Locate every blood parasite and identify its species.
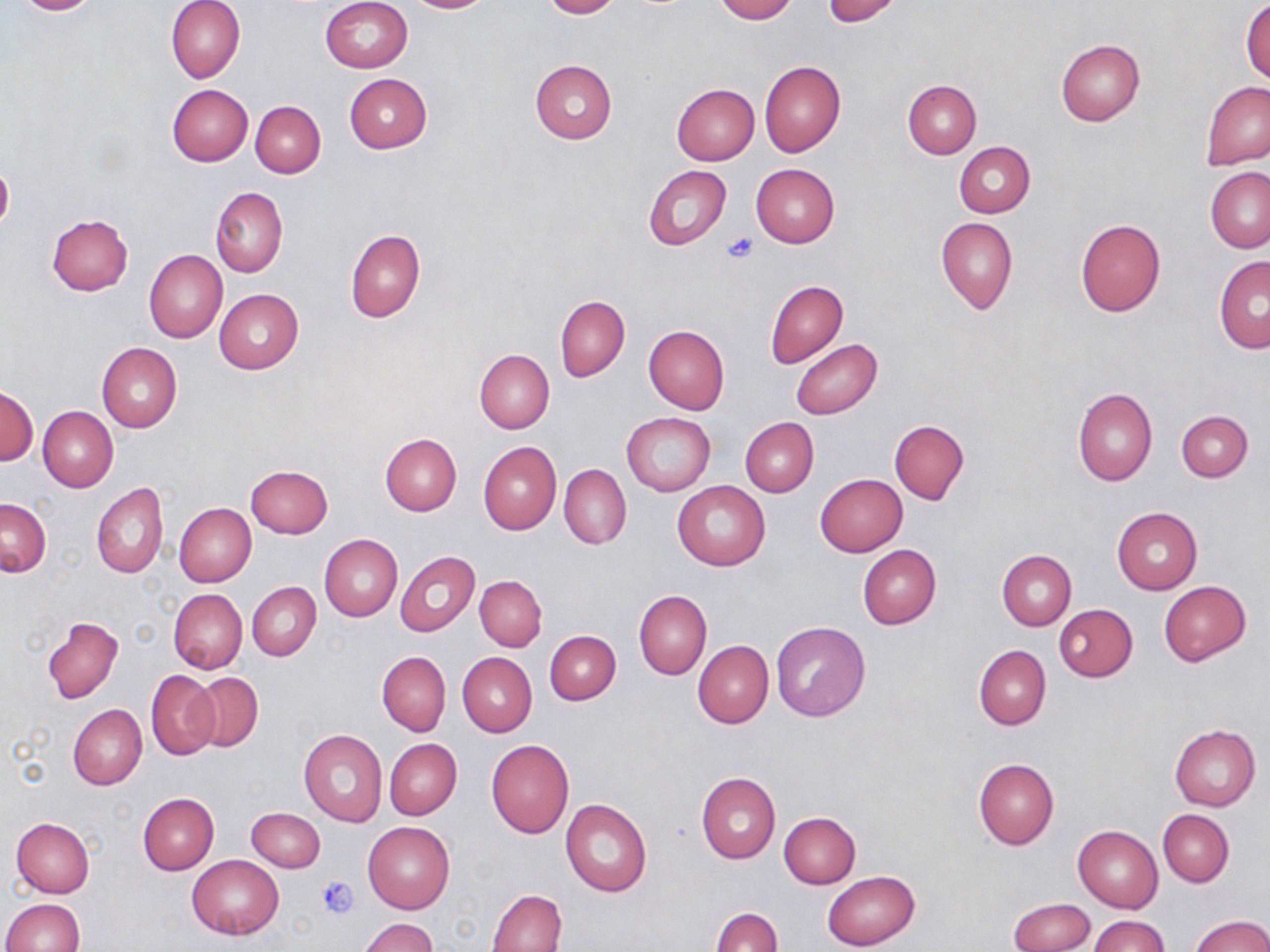
No blood parasites seen.

Approximate bounding boxes as (x1, y1, x2, y2) in pixels. Platelet locations: (722, 232, 759, 264), (317, 874, 359, 917). Uninfected red blood cell locations: (11, 0, 103, 15), (166, 0, 245, 83), (320, 0, 413, 73), (404, 0, 494, 14), (540, 0, 621, 19), (713, 0, 797, 22), (823, 0, 902, 25), (1241, 2, 1270, 83), (1054, 39, 1143, 126), (530, 60, 617, 144), (759, 61, 845, 157), (343, 74, 431, 154), (902, 80, 981, 159), (1201, 82, 1270, 170), (167, 84, 253, 166), (672, 84, 760, 165), (250, 100, 325, 178), (955, 142, 1035, 218), (0, 162, 14, 231), (750, 163, 839, 247), (644, 165, 731, 250), (1206, 168, 1270, 253), (210, 186, 288, 277), (47, 215, 133, 295), (936, 217, 1018, 313), (1075, 219, 1165, 317), (345, 229, 425, 323), (144, 249, 227, 343), (1213, 257, 1270, 354), (765, 280, 847, 368), (214, 289, 303, 374), (555, 295, 630, 381), (643, 325, 729, 415), (790, 339, 883, 418), (97, 343, 181, 433), (474, 348, 555, 433), (0, 386, 38, 465), (1072, 388, 1157, 486), (37, 406, 117, 492), (1177, 410, 1252, 482), (623, 412, 714, 497), (741, 417, 819, 497), (890, 419, 969, 506), (380, 434, 461, 515), (478, 441, 561, 535), (560, 464, 631, 550), (245, 465, 333, 538), (815, 473, 907, 557), (673, 480, 770, 571), (91, 483, 168, 578), (1, 497, 51, 576), (175, 502, 256, 587), (1111, 507, 1203, 595), (319, 534, 402, 621), (858, 544, 941, 629), (394, 550, 479, 637), (997, 551, 1075, 630), (475, 576, 546, 651), (1159, 581, 1251, 665), (247, 583, 320, 661), (169, 589, 248, 673), (634, 591, 711, 679), (1053, 603, 1138, 681), (43, 617, 124, 704), (770, 620, 871, 722), (544, 630, 620, 704), (693, 641, 773, 728), (974, 645, 1050, 729), (377, 652, 450, 736), (457, 652, 536, 737), (146, 670, 219, 761), (191, 672, 263, 752), (67, 705, 147, 790), (1169, 723, 1260, 811), (298, 729, 388, 827), (385, 738, 462, 820), (486, 740, 574, 839), (972, 758, 1059, 850), (697, 771, 780, 863), (138, 793, 218, 874), (560, 799, 653, 897), (246, 807, 325, 872), (1158, 809, 1234, 887), (779, 812, 861, 888), (11, 817, 95, 897), (363, 821, 455, 914), (1073, 825, 1163, 912), (187, 854, 283, 939), (822, 870, 920, 950), (488, 889, 567, 952), (1, 898, 84, 951), (1009, 898, 1094, 951), (711, 907, 783, 952), (1190, 914, 1270, 952), (1089, 916, 1169, 952), (360, 918, 437, 952). Slide-level diagnosis: no evidence of blood parasites. Optical microscopy. Captured at 1000x magnification. Thin blood smear. One field of a larger specimen. May-Grünwald-Giemsa stain. Image is 1270×952 pixels.